Locate every Plasmodium parasite.
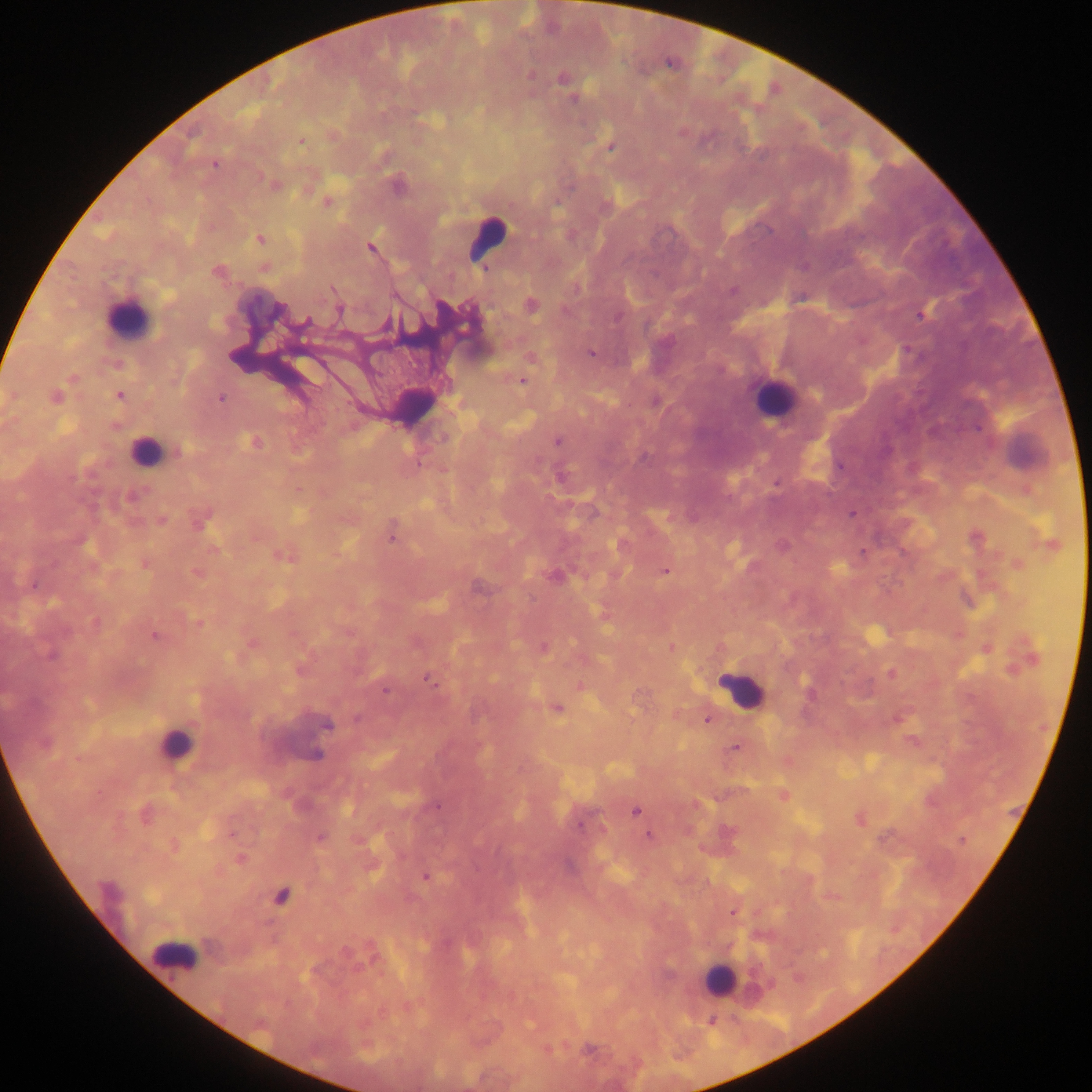
Approximate centers as {x, y} in pixels.
Plasmodium parasites: {562, 79}, {573, 100}, {302, 141}, {611, 147}, {214, 165}, {274, 184}, {398, 186}, {327, 203}, {260, 239}, {371, 248}, {217, 271}, {333, 289}, {733, 291}, {532, 305}, {278, 310}, {339, 310}, {921, 314}, {617, 317}, {306, 322}, {386, 325}, {590, 353}, {522, 381}, {120, 396}, {55, 397}, {221, 398}, {444, 438}, {558, 441}, {254, 442}, {180, 451}, {419, 464}, {776, 483}, {131, 496}, {852, 514}, {162, 520}, {200, 522}, {391, 538}, {215, 550}, {863, 553}, {285, 557}, {145, 564}, {665, 571}, {197, 573}, {554, 576}, {33, 585}, {198, 622}, {96, 623}, {154, 636}, {544, 648}, {671, 648}, {51, 656}, {891, 674}, {428, 679}, {385, 691}, {557, 709}, {357, 718}, {707, 720}, {327, 725}, {45, 744}, {735, 747}, {317, 755}, {438, 807}, {636, 811}, {580, 826}, {649, 837}, {320, 838}, {961, 840}, {241, 859}, {425, 877}, {109, 890}, {281, 896}, {734, 913}.

Leukocyte locations: {488, 238}, {128, 318}, {772, 396}, {144, 450}, {741, 690}, {174, 744}, {172, 954}, {717, 980}. Image is 1092×1092 pixels. Photographed through a microscope with a mobile-phone camera. Collected in Ghana. Thick blood smear. One field of view.